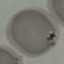

{
  "malaria_status": "uninfected",
  "stain": "Giemsa",
  "image_type": "automatically extracted cell patch, resized to 64 × 64 pixels",
  "preparation": "thin blood film",
  "capture": "smartphone camera at the microscope eyepiece"
}